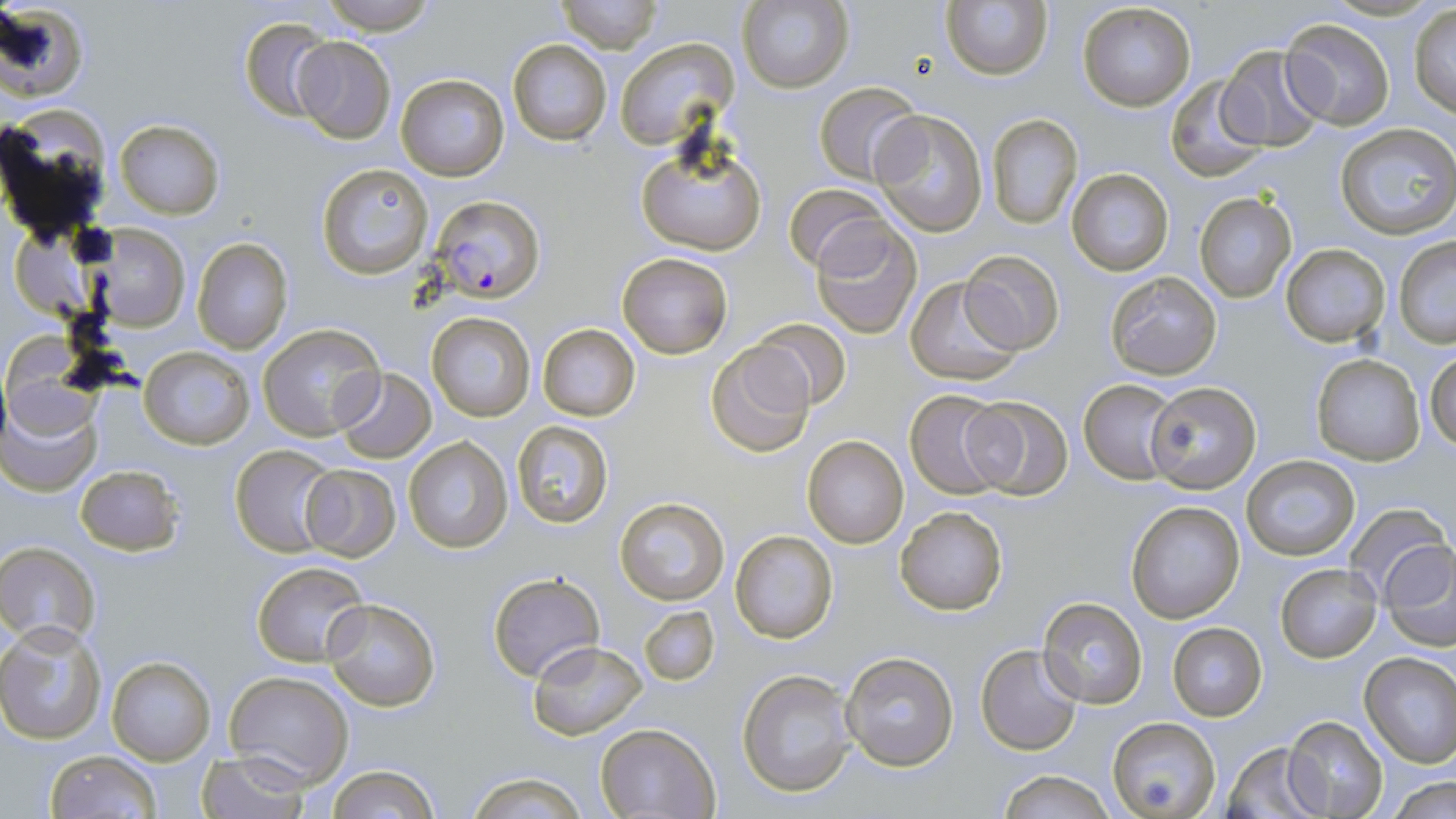

Plasmodium falciparum-infected red blood cell locations = approximate bounding boxes as (x1, y1, x2, y2) in pixels: (434, 196, 543, 306)
slide-level diagnosis = Plasmodium falciparum
magnification = 1000x
image size = 1456×819 pixels
field of view = single
uninfected red blood cell locations = approximate bounding boxes as (x1, y1, x2, y2) in pixels: (319, 0, 437, 35), (551, 0, 665, 50), (737, 0, 853, 94), (0, 1, 88, 101), (941, 2, 1053, 81), (1076, 2, 1197, 113), (1410, 4, 1456, 118), (240, 17, 334, 120), (1280, 18, 1396, 128), (290, 36, 395, 145), (507, 38, 611, 146), (615, 38, 737, 148), (1217, 45, 1328, 151), (395, 72, 509, 182), (1164, 75, 1270, 182), (813, 80, 923, 185), (0, 104, 115, 243), (871, 109, 989, 237), (987, 114, 1082, 229), (114, 118, 224, 220), (1334, 123, 1456, 239), (637, 141, 767, 256), (315, 163, 434, 279), (1065, 167, 1175, 277), (785, 183, 892, 275), (1193, 192, 1296, 303), (811, 218, 924, 340), (92, 224, 189, 330), (1392, 238, 1456, 347), (191, 239, 294, 355), (1280, 245, 1390, 348), (958, 250, 1066, 354), (617, 253, 733, 359), (1104, 270, 1222, 380), (904, 275, 1025, 385), (427, 311, 535, 421), (747, 316, 853, 410), (257, 324, 384, 441), (537, 324, 640, 421), (704, 341, 817, 458), (139, 346, 253, 449), (1427, 350, 1456, 452), (1310, 354, 1424, 464), (332, 367, 437, 463), (1148, 379, 1263, 494), (1079, 380, 1181, 484), (904, 390, 1014, 498), (2, 391, 102, 496), (962, 396, 1075, 499), (509, 421, 615, 530), (802, 435, 910, 549), (403, 436, 514, 554), (230, 444, 338, 557), (1241, 456, 1360, 561), (75, 464, 184, 556), (299, 464, 401, 561), (614, 496, 730, 605), (1126, 499, 1245, 623), (894, 504, 1010, 617), (1345, 504, 1453, 608), (730, 529, 840, 644), (1380, 539, 1456, 646), (0, 542, 100, 645), (253, 561, 371, 668), (1276, 565, 1380, 662), (488, 571, 605, 683), (1038, 598, 1147, 709), (323, 600, 440, 712), (635, 603, 720, 688), (1167, 621, 1267, 721), (1, 622, 106, 745), (528, 640, 648, 739), (975, 644, 1085, 755), (840, 651, 959, 770), (1359, 651, 1456, 767), (106, 654, 216, 765), (736, 667, 858, 799), (225, 670, 354, 787), (1282, 715, 1390, 819), (1107, 718, 1220, 819), (597, 722, 720, 819), (1220, 740, 1329, 819), (44, 750, 162, 819), (197, 751, 311, 819), (325, 765, 439, 819), (997, 769, 1115, 819), (464, 771, 590, 818), (1385, 778, 1455, 819)
stain = May-Grünwald-Giemsa
preparation = thin blood smear
modality = optical microscopy